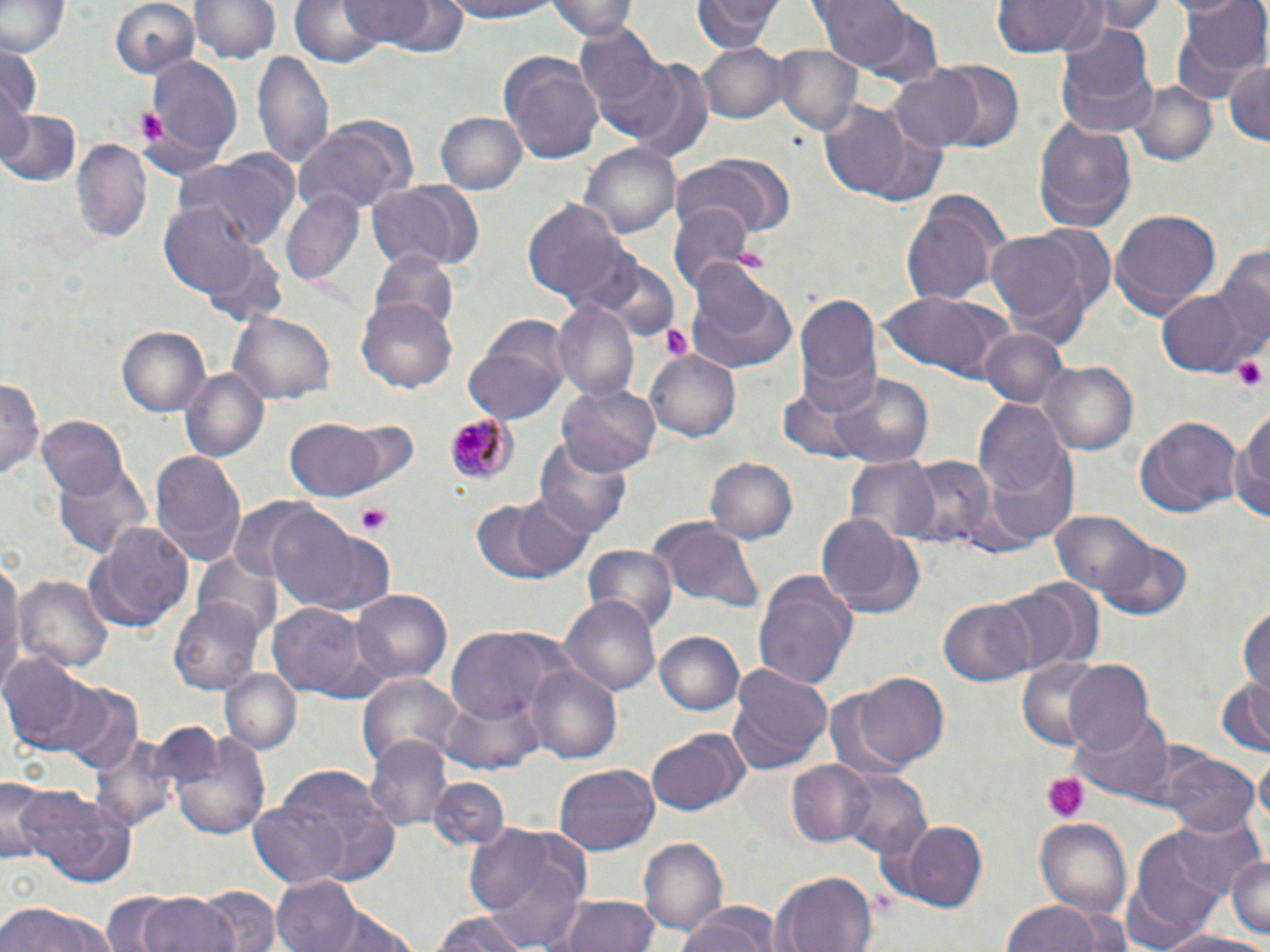
{
  "slide_level_diagnosis": "Plasmodium malariae",
  "platelet_locations": "approximate bounding boxes as [x1, y1, x2, y2] in pixels: [135, 105, 172, 147], [1232, 353, 1268, 395], [355, 503, 393, 535], [1043, 773, 1089, 820]",
  "magnification": "1000x",
  "image_size": "1270×952 pixels",
  "preparation": "thin blood film",
  "modality": "optical microscopy",
  "field_of_view": "single",
  "plasmodium_malariae_infected_red_blood_cell_locations": "approximate bounding boxes as [x1, y1, x2, y2] in pixels: [441, 410, 514, 490]",
  "stain": "May-Grünwald-Giemsa",
  "uninfected_red_blood_cell_locations": "approximate bounding boxes as [x1, y1, x2, y2] in pixels: [192, 0, 281, 65], [290, 0, 389, 71], [434, 0, 569, 24], [548, 0, 640, 41], [692, 0, 782, 53], [809, 0, 923, 76], [989, 0, 1102, 59], [1089, 0, 1165, 35], [1167, 0, 1265, 100], [0, 1, 68, 58], [107, 1, 201, 80], [340, 1, 440, 48], [573, 23, 663, 115], [1055, 23, 1158, 136], [0, 44, 42, 121], [698, 44, 789, 123], [772, 44, 861, 137], [253, 48, 335, 169], [498, 50, 603, 164], [142, 53, 244, 171], [612, 55, 715, 162], [1225, 60, 1270, 146], [930, 61, 1025, 153], [889, 69, 983, 152], [1127, 80, 1217, 166], [818, 102, 913, 198], [2, 107, 80, 188], [435, 111, 526, 196], [1031, 114, 1137, 230], [293, 116, 415, 214], [71, 135, 152, 244], [578, 140, 681, 242], [672, 155, 793, 238], [172, 160, 293, 250], [367, 178, 487, 274], [281, 189, 365, 286], [900, 192, 1006, 308], [521, 197, 634, 310], [160, 201, 268, 300], [669, 202, 753, 296], [1109, 209, 1220, 320], [1030, 223, 1117, 314], [988, 232, 1088, 330], [1213, 243, 1270, 359], [367, 249, 462, 334], [581, 254, 681, 339], [684, 266, 799, 376], [1157, 289, 1245, 377], [878, 291, 1010, 383], [794, 292, 882, 416], [551, 297, 639, 403], [357, 298, 457, 393], [228, 312, 337, 406], [117, 326, 211, 417], [980, 327, 1068, 409], [464, 345, 567, 424], [645, 346, 741, 440], [1040, 360, 1137, 455], [176, 368, 269, 463], [830, 372, 935, 467], [1, 376, 42, 484], [777, 383, 870, 460], [558, 384, 660, 476], [974, 400, 1072, 505], [1231, 408, 1270, 531], [1132, 415, 1241, 518], [37, 416, 130, 502], [334, 418, 421, 494], [283, 420, 386, 499], [534, 434, 634, 542], [151, 449, 245, 566], [705, 456, 798, 545], [844, 456, 940, 544], [903, 456, 996, 550], [56, 463, 152, 561], [468, 495, 593, 583], [266, 508, 388, 613], [1052, 510, 1152, 596], [817, 513, 911, 609], [647, 517, 766, 608], [87, 520, 193, 630], [1098, 533, 1189, 619], [581, 544, 677, 637], [193, 556, 282, 637], [0, 557, 25, 696], [15, 571, 114, 672], [754, 572, 855, 687], [994, 585, 1082, 673], [351, 590, 451, 684], [168, 596, 264, 697], [562, 596, 660, 698], [939, 597, 1036, 687], [1238, 600, 1270, 695], [269, 605, 371, 699], [447, 629, 558, 728], [654, 631, 745, 718], [4, 654, 101, 752], [1017, 659, 1107, 752], [1063, 661, 1157, 756], [526, 663, 622, 763], [728, 664, 832, 773], [220, 668, 302, 754], [357, 673, 463, 774], [850, 673, 948, 772], [1214, 674, 1270, 755], [64, 687, 142, 776], [823, 690, 912, 784], [440, 694, 542, 773], [1070, 713, 1175, 801], [164, 726, 275, 841], [89, 729, 183, 835], [644, 734, 741, 818], [363, 738, 451, 831], [1167, 753, 1257, 837], [1257, 754, 1270, 831], [785, 758, 880, 849], [553, 764, 660, 855], [836, 767, 931, 862], [263, 770, 402, 885], [1, 778, 49, 868], [426, 778, 510, 854], [12, 786, 132, 887], [434, 786, 535, 895], [251, 799, 352, 887], [1168, 809, 1266, 898], [1036, 817, 1132, 921], [889, 818, 988, 911], [460, 823, 593, 947], [1126, 828, 1240, 942], [639, 836, 727, 932], [1226, 854, 1270, 941], [770, 869, 879, 952], [270, 874, 363, 950], [200, 886, 280, 952], [138, 892, 236, 952], [547, 894, 664, 952], [1002, 897, 1108, 952], [0, 900, 118, 952], [675, 905, 781, 952], [428, 908, 538, 952], [317, 909, 419, 952], [1157, 928, 1270, 952]"
}